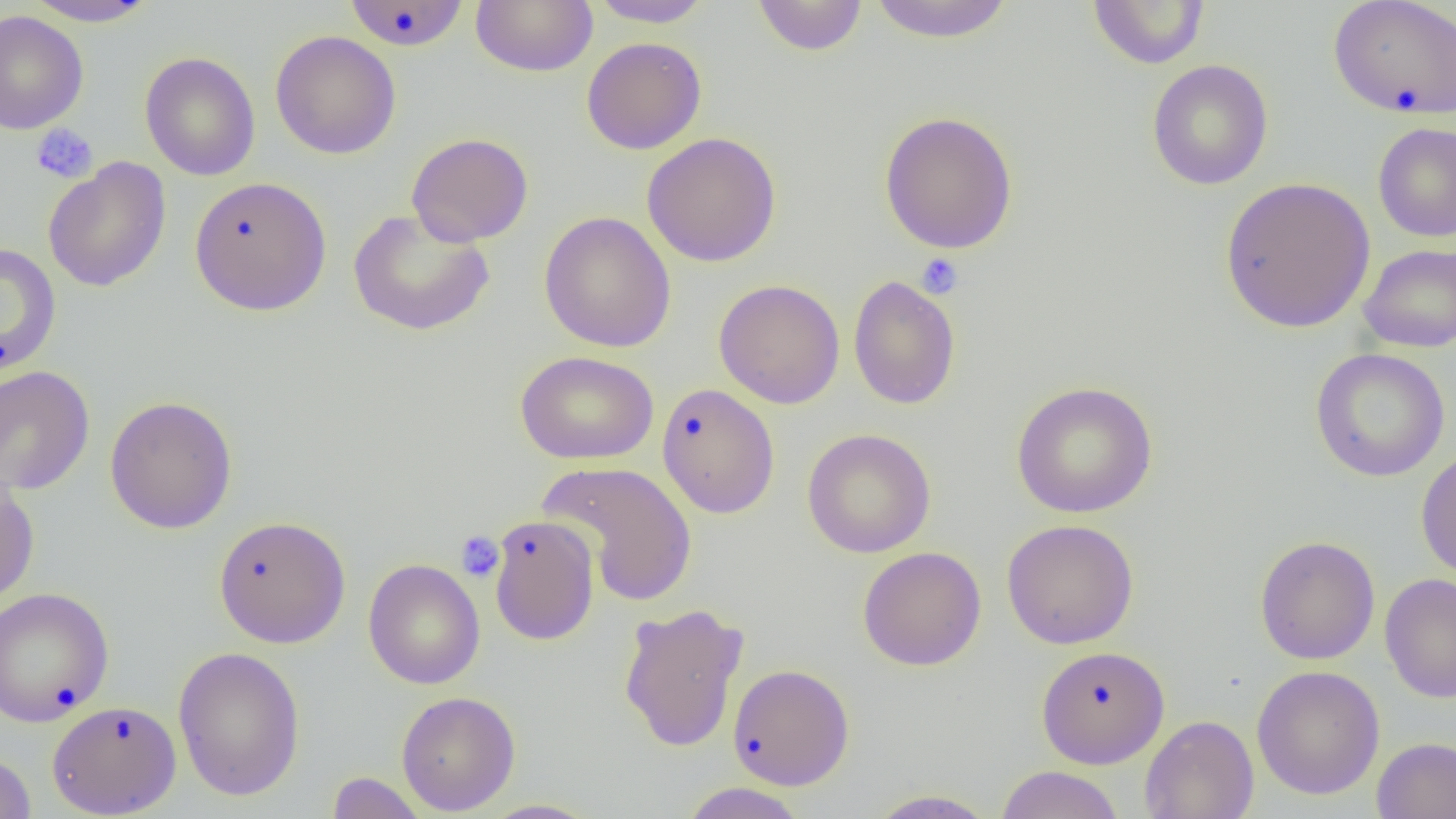

slide_level_diagnosis: negative for blood parasites
uninfected_red_blood_cell_locations: 'approximate bounding boxes as (x1,y1)-(x2,y2) corner pairs in pixels: (21,0)-(162,27), (343,0)-(471,51), (470,0)-(598,77), (752,0)-(868,56), (866,0)-(1015,43), (587,1)-(716,28), (1087,1)-(1210,69), (1328,1)-(1456,119), (0,10)-(89,135), (270,30)-(401,159), (581,37)-(707,155), (139,52)-(261,181), (1146,59)-(1274,190), (878,110)-(1019,254), (1372,121)-(1456,243), (406,132)-(534,247), (641,132)-(782,267), (43,158)-(171,292), (189,176)-(331,315), (1218,176)-(1376,333), (348,208)-(496,336), (539,211)-(676,353), (0,242)-(61,376), (1359,243)-(1456,352), (847,274)-(961,410), (714,279)-(845,409), (1310,348)-(1450,482), (515,350)-(659,465), (0,366)-(95,496), (1011,380)-(1158,518), (657,383)-(780,518), (104,395)-(238,535), (802,428)-(936,558), (1416,447)-(1456,582), (538,460)-(698,607), (0,472)-(40,609), (213,515)-(351,648), (488,515)-(600,645), (1001,518)-(1139,650), (1254,535)-(1380,665), (857,546)-(986,671), (363,559)-(485,689), (1380,573)-(1456,704), (0,587)-(114,726), (618,602)-(749,752), (1036,645)-(1170,768), (172,646)-(306,801), (728,663)-(855,790), (1251,664)-(1385,800), (396,691)-(520,815), (46,700)-(182,817), (1139,714)-(1259,819), (1371,736)-(1456,819), (0,751)-(36,818), (995,765)-(1125,819), (327,772)-(427,818), (678,782)-(810,819), (865,789)-(1000,818), (476,799)-(602,818)'
platelet_locations: 'approximate bounding boxes as (x1,y1)-(x2,y2) corner pairs in pixels: (30,123)-(98,184), (916,253)-(964,299), (456,531)-(504,582)'
magnification: 1000x
field_of_view: one of a larger specimen
preparation: thin blood film
image_size: 1456×819 pixels
modality: light microscopy